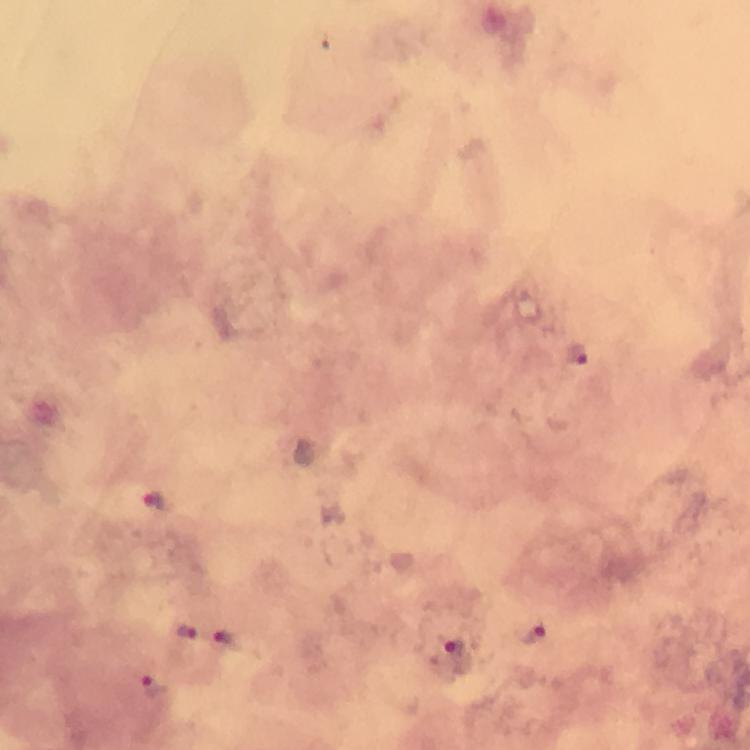

Approximate centers as {x, y} in pixels. Plasmodium parasite locations: {577, 355}, {154, 499}, {187, 633}, {535, 635}, {226, 638}, {454, 654}, {153, 687}. Thick smear. Image is 750×750 pixels. At 100x magnification. From a diagnostic examination for malaria. Immersion oil applied. Giemsa-stained preparation. A crop from one field of view. Photographed with a smartphone mounted on the microscope.